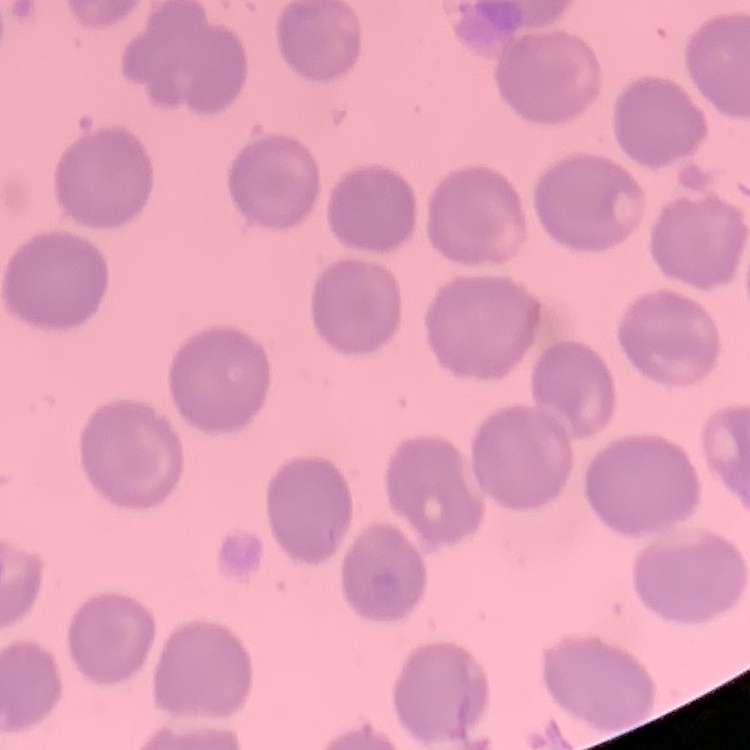 The red blood cells exhibit no rouleaux formation. Thin blood smear. Square crop of a larger photomicrograph. Field's or Giemsa stain.